Give the position of every Plasmodium parasite visible.
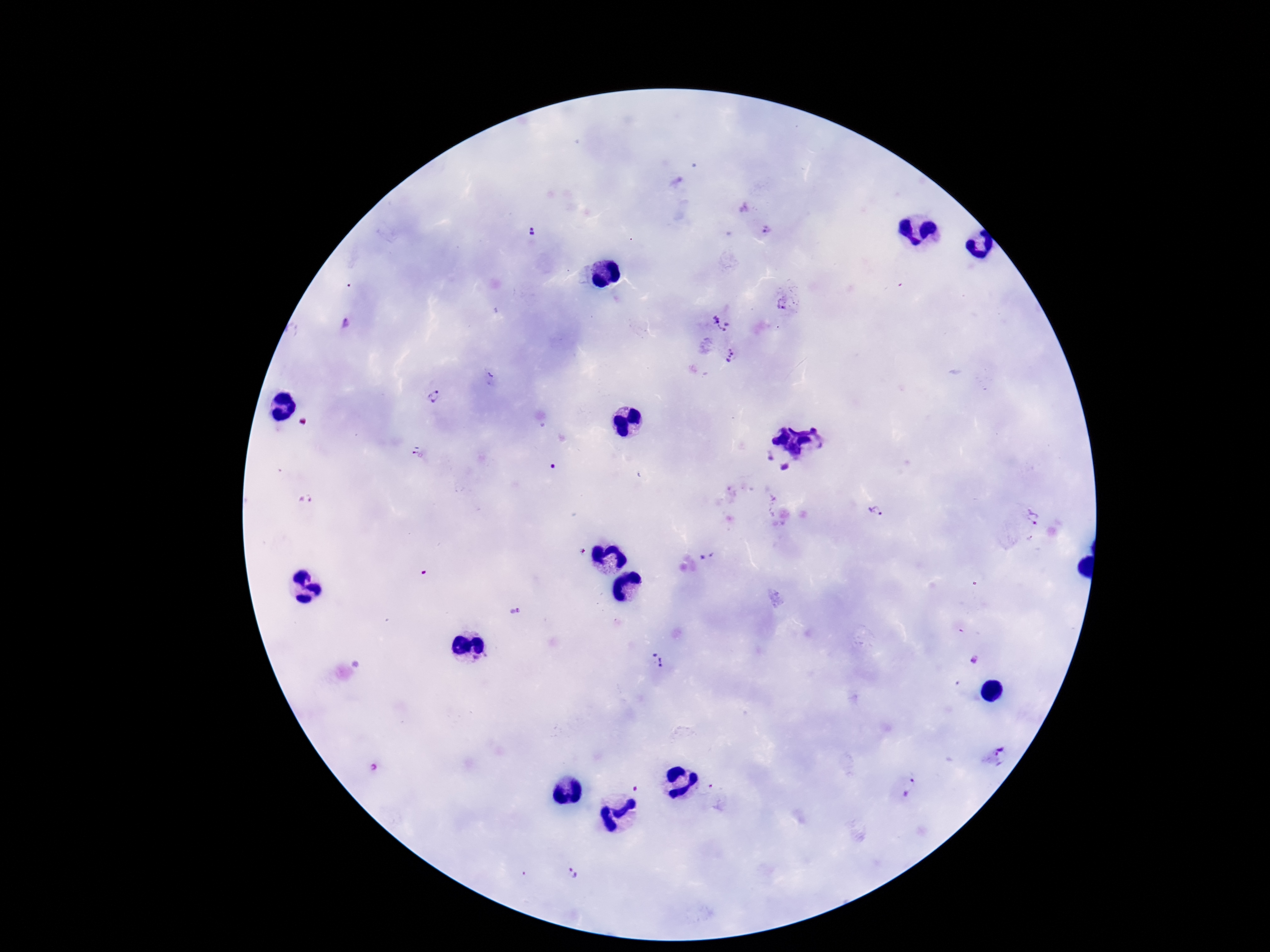
Approximate centers as {x, y} in pixels.
Plasmodium parasites: {767, 231}, {530, 233}, {783, 304}, {347, 324}, {721, 324}, {732, 356}, {435, 397}, {419, 455}, {767, 457}, {784, 467}, {874, 511}, {1027, 519}, {707, 557}, {516, 611}, {658, 659}, {975, 660}, {998, 757}, {911, 788}, {574, 874}.

One field from this slide. Image is 1270×952 pixels. Smartphone photograph taken through the microscope eyepiece. Thick peripheral-blood smear. Patient malaria status: infected. 100x magnification. Giemsa stain.